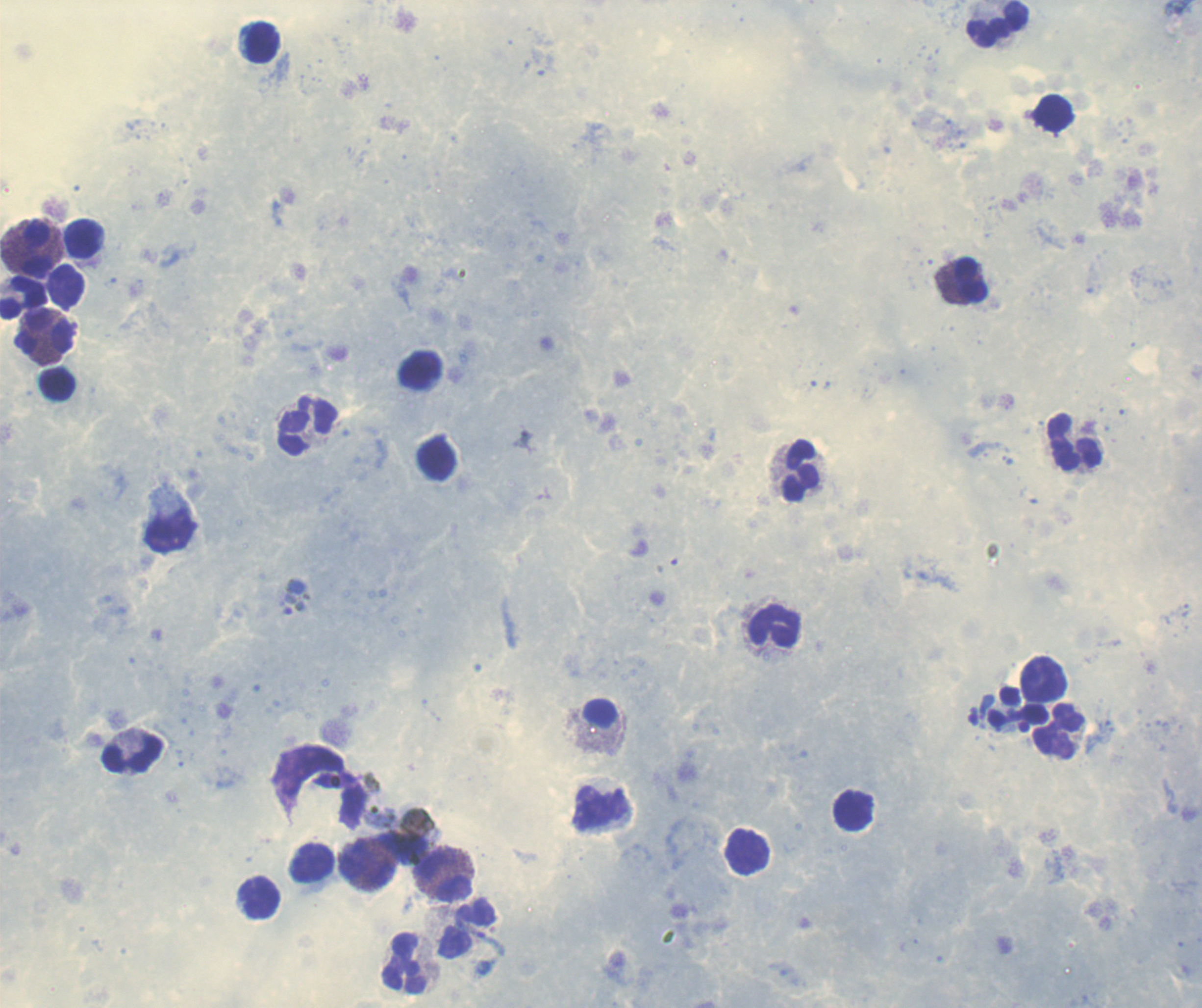
Approximate centers as (x, y) in pixels. Gametocyte locations: (294, 596). Leukocyte locations: (997, 24), (262, 42), (83, 238), (36, 248), (969, 279), (23, 298), (44, 337), (58, 384), (308, 426), (1074, 441), (802, 470), (171, 529), (774, 625), (1043, 679), (1059, 732), (132, 753), (600, 808), (313, 862), (368, 865), (443, 877), (260, 898), (466, 929), (405, 963). Coloration quality: good. Image is 1202×1008 pixels. One field from this slide. Romanowsky-stained preparation. Captured at 100x magnification. Background quality: good. Thick smear of blood. Previously used in a real diagnosis. Result: positive for Plasmodium parasites.